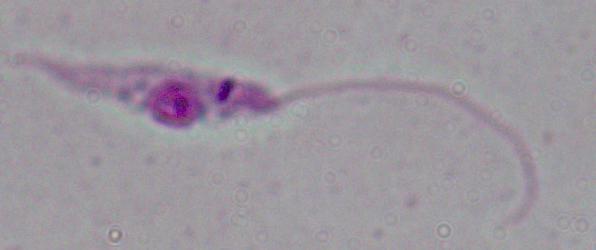 Micrograph. A Leishmania parasite is seen. 1000x magnification.